Assess this cell for malaria.
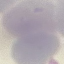

Uninfected.

image_type: automatically extracted cell patch, resized to 64 × 64 pixels
capture: smartphone camera at the microscope eyepiece
preparation: thin blood smear
stain: Giemsa